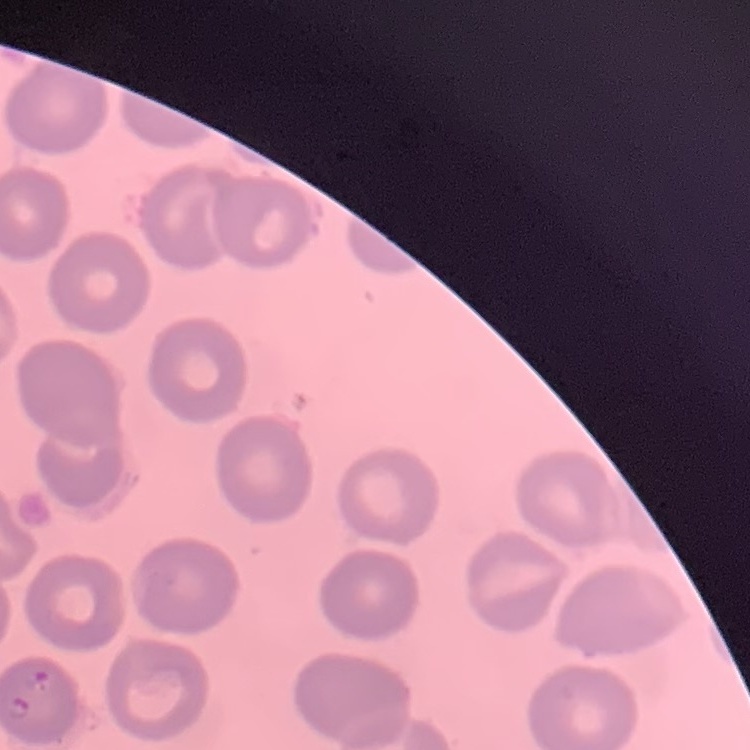

erythrocyte morphology = no rouleaux formation
image type = one tile cut from a larger photomicrograph
preparation = thin blood smear
stain = Field's or Giemsa